Describe the morphology of the erythrocytes.
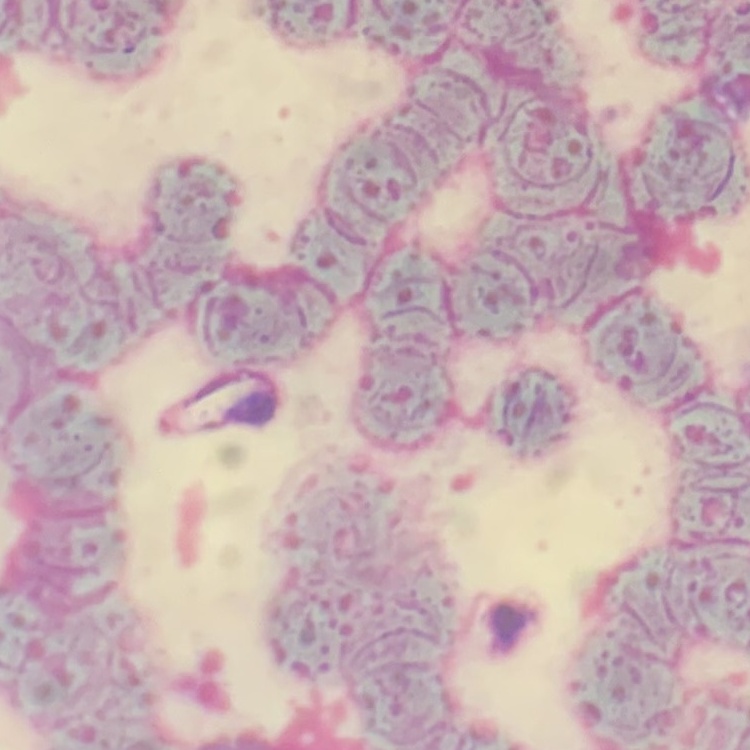

They show rouleaux formation.

Summary:
  - Image type: square crop of a larger photomicrograph
  - Preparation: thin blood smear
  - Stain: Field's or Giemsa